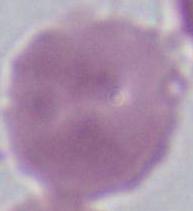

A red blood cell is seen. Micrograph. Captured at 1000x magnification.